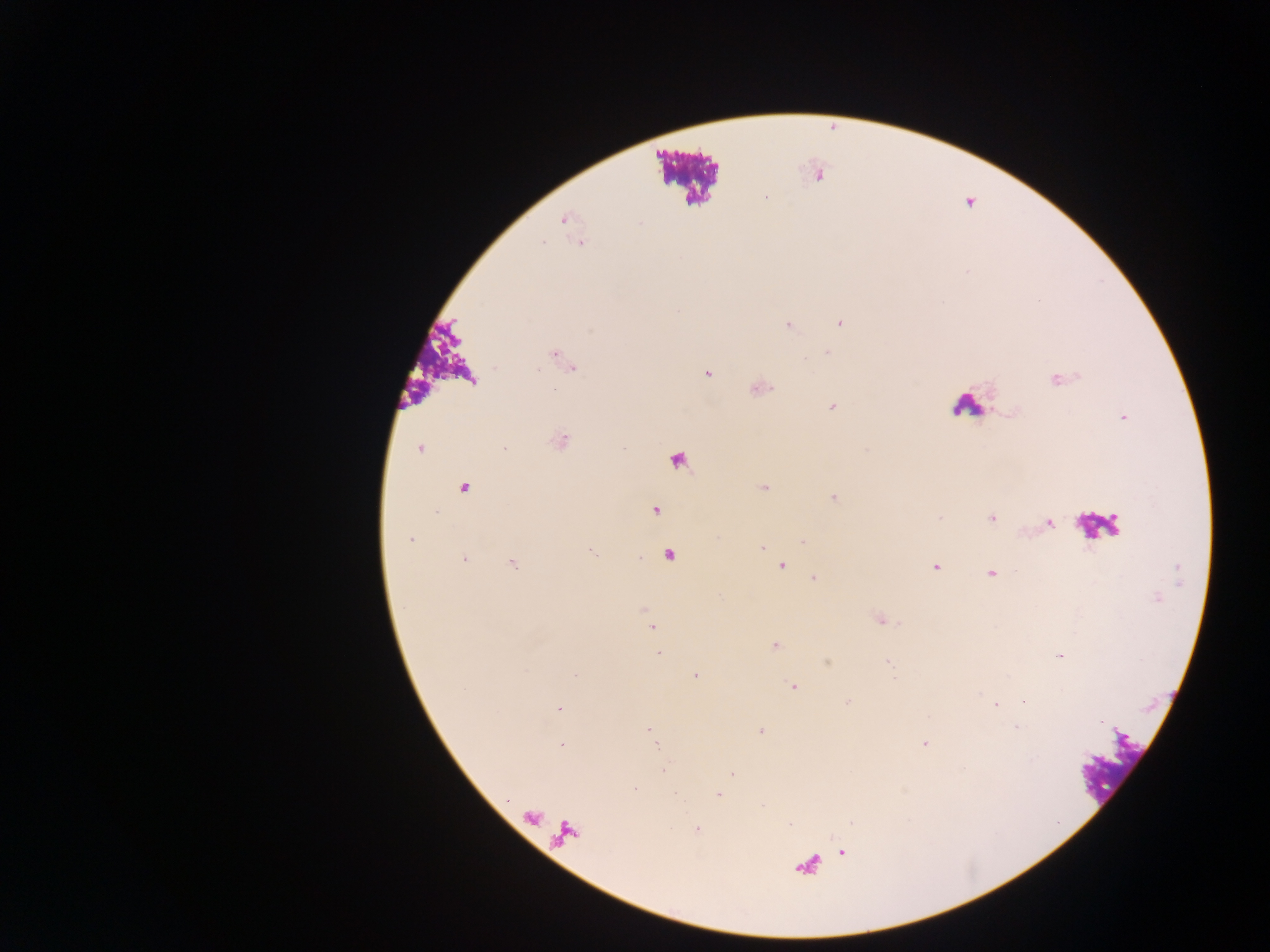

Approximate centers as (x, y) in pixels.
Summary:
  - Leukocyte locations: (685, 174), (967, 406), (679, 460), (1101, 526)
  - Plasmodium parasite locations: (766, 197), (563, 219), (640, 223), (542, 243), (840, 323), (788, 327), (827, 353), (707, 373), (1060, 380), (554, 389), (833, 406), (562, 442), (419, 449), (504, 449), (763, 487), (463, 488), (834, 497), (654, 510), (939, 517), (992, 518), (1049, 523), (410, 539), (803, 541), (763, 547), (592, 551), (668, 556), (464, 560), (512, 564), (781, 565), (935, 568), (991, 573), (813, 578), (1157, 598), (645, 612), (651, 627), (775, 646), (659, 653), (1060, 655), (887, 662), (574, 675), (695, 675), (793, 687), (847, 702), (996, 704), (558, 708), (1016, 727), (648, 730), (761, 731), (654, 739), (923, 744), (562, 745), (664, 769), (732, 774), (634, 788), (718, 794), (790, 824), (696, 829), (842, 852)
  - Field of view: single
  - Image size: 1270×952 pixels
  - Country: Ghana
  - Capture: mobile-phone photograph through a microscope
  - Preparation: thick blood smear